Assess this cell for malaria.
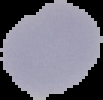

It is uninfected.

image_type: cell region segmented out of the field of view; surrounding area masked to black
image_size: 103×100 pixels
preparation: thin blood smear